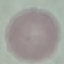

Result: negative for malaria parasites. Giemsa stain. Cell patch, automatically extracted from a larger field of view and resized to 64 × 64 pixels. Thin smear of blood. Acquired by smartphone through the microscope eyepiece.